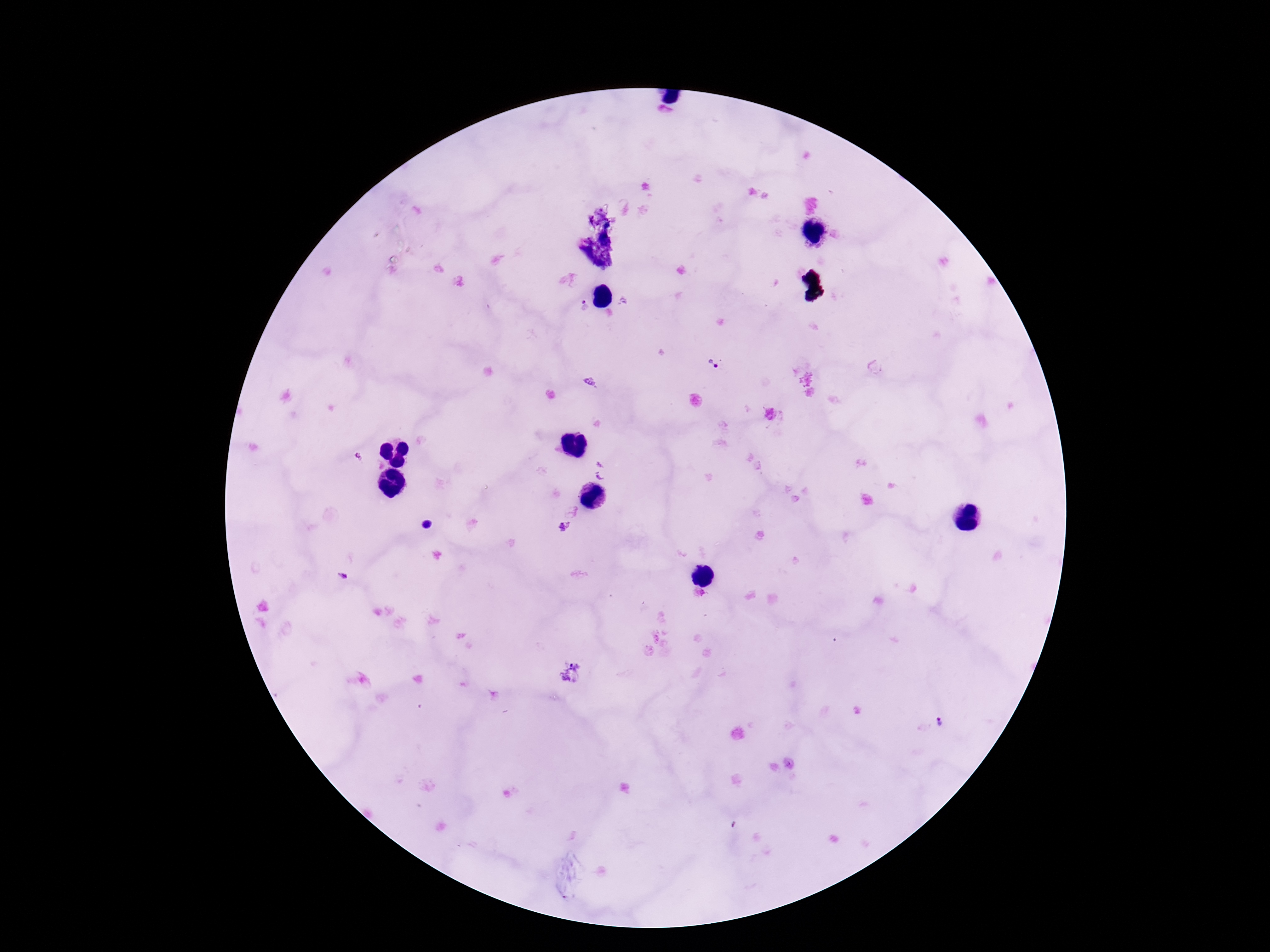
stain: Giemsa
capture: smartphone camera through the microscope eyepiece
preparation: thick blood film
field_of_view: one from this slide
magnification: 100x
image_size: 1270×952 pixels
patient_malaria_status: infected
plasmodium_parasite_locations: 'approximate centers as (x, y) in pixels: (584, 307), (713, 365), (563, 527), (344, 577), (940, 721)'